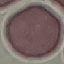

Summary:
  - Result: no malaria parasites seen
  - Image type: cell patch, automatically extracted from a larger field of view and resized to 64 × 64 pixels
  - Stain: Giemsa
  - Preparation: thin blood smear
  - Capture: smartphone camera at the microscope eyepiece